Locate every Plasmodium falciparum-infected red blood cell.
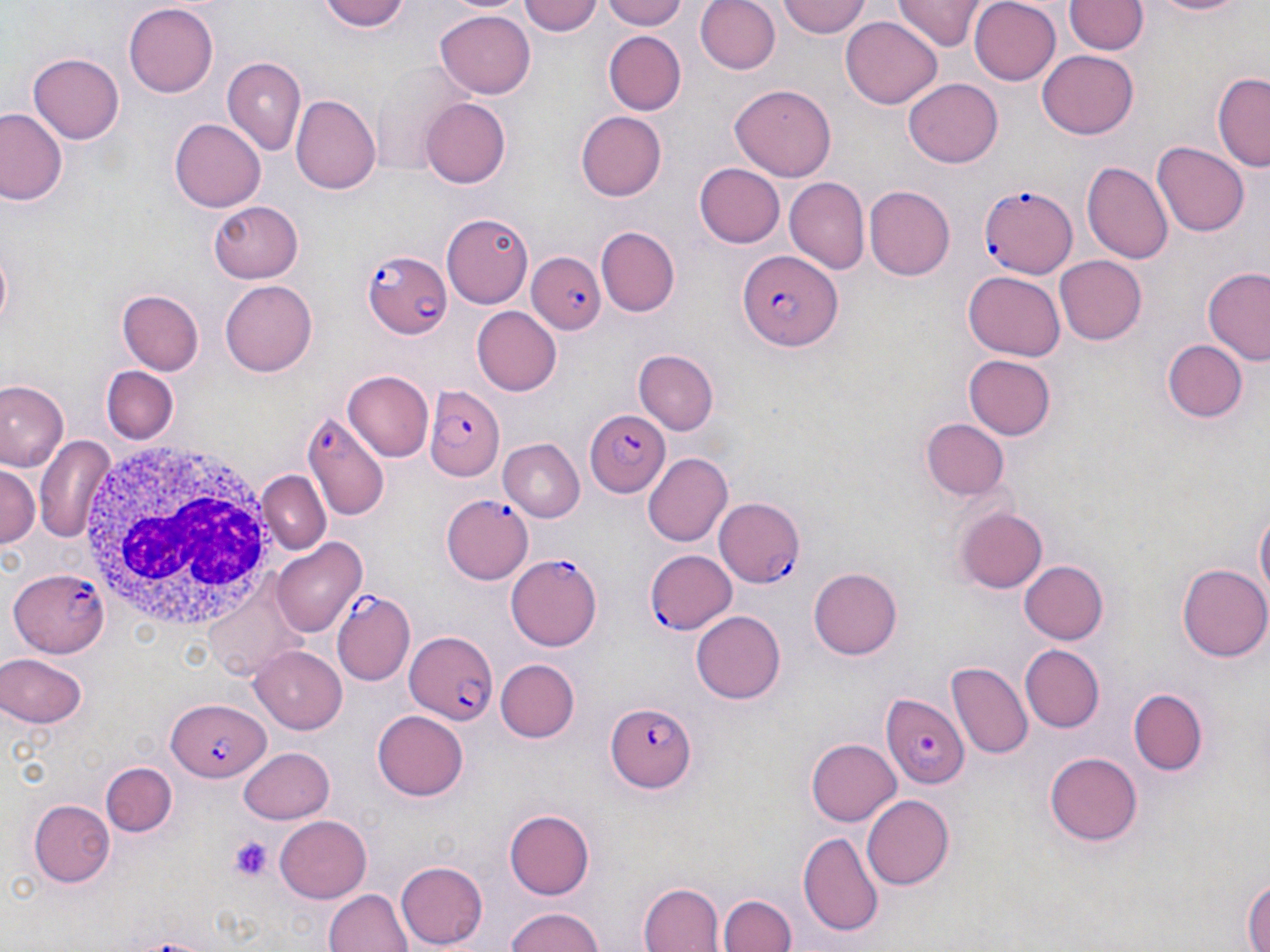

Approximate bounding boxes as named x1/y1/x2/y2 corners in pixels.
Plasmodium falciparum-infected red blood cells: (x1=979, y1=183, x2=1078, y2=278), (x1=364, y1=249, x2=453, y2=339), (x1=525, y1=250, x2=605, y2=336), (x1=735, y1=251, x2=840, y2=353), (x1=429, y1=389, x2=505, y2=481), (x1=582, y1=410, x2=670, y2=498), (x1=302, y1=416, x2=388, y2=524), (x1=441, y1=494, x2=534, y2=584), (x1=714, y1=498, x2=808, y2=588), (x1=644, y1=549, x2=737, y2=635), (x1=505, y1=555, x2=604, y2=651), (x1=7, y1=567, x2=110, y2=655), (x1=333, y1=592, x2=415, y2=686), (x1=402, y1=628, x2=498, y2=727), (x1=883, y1=694, x2=969, y2=789), (x1=167, y1=701, x2=267, y2=782), (x1=607, y1=701, x2=696, y2=793).

White blood cell locations: (x1=76, y1=436, x2=285, y2=636). Uninfected red blood cell locations: (x1=320, y1=0, x2=414, y2=33), (x1=519, y1=0, x2=604, y2=38), (x1=600, y1=0, x2=692, y2=29), (x1=695, y1=0, x2=780, y2=75), (x1=777, y1=0, x2=871, y2=38), (x1=896, y1=0, x2=983, y2=51), (x1=967, y1=0, x2=1061, y2=85), (x1=1147, y1=0, x2=1251, y2=18), (x1=1066, y1=1, x2=1146, y2=57), (x1=121, y1=3, x2=220, y2=98), (x1=436, y1=9, x2=535, y2=97), (x1=841, y1=16, x2=943, y2=109), (x1=601, y1=29, x2=687, y2=116), (x1=1037, y1=50, x2=1139, y2=140), (x1=29, y1=55, x2=123, y2=143), (x1=222, y1=57, x2=305, y2=155), (x1=367, y1=63, x2=480, y2=176), (x1=1212, y1=71, x2=1269, y2=170), (x1=903, y1=77, x2=1003, y2=168), (x1=731, y1=85, x2=837, y2=181), (x1=292, y1=94, x2=381, y2=194), (x1=421, y1=97, x2=510, y2=188), (x1=0, y1=109, x2=66, y2=207), (x1=575, y1=111, x2=668, y2=200), (x1=170, y1=118, x2=265, y2=211), (x1=1153, y1=141, x2=1249, y2=237), (x1=1084, y1=160, x2=1175, y2=265), (x1=694, y1=162, x2=783, y2=246), (x1=785, y1=177, x2=869, y2=274), (x1=865, y1=186, x2=955, y2=281), (x1=209, y1=197, x2=304, y2=281), (x1=442, y1=210, x2=533, y2=308), (x1=598, y1=225, x2=679, y2=316), (x1=1056, y1=253, x2=1146, y2=343), (x1=1200, y1=264, x2=1270, y2=364), (x1=961, y1=271, x2=1066, y2=361), (x1=221, y1=280, x2=317, y2=377), (x1=118, y1=289, x2=203, y2=375), (x1=472, y1=307, x2=562, y2=397), (x1=1162, y1=339, x2=1247, y2=423), (x1=633, y1=349, x2=719, y2=436), (x1=963, y1=352, x2=1056, y2=439), (x1=101, y1=368, x2=177, y2=445), (x1=342, y1=370, x2=434, y2=463), (x1=0, y1=380, x2=66, y2=472), (x1=921, y1=419, x2=1008, y2=500), (x1=35, y1=432, x2=116, y2=546), (x1=501, y1=439, x2=585, y2=521), (x1=644, y1=453, x2=732, y2=547), (x1=0, y1=464, x2=40, y2=551), (x1=258, y1=471, x2=330, y2=555), (x1=1253, y1=504, x2=1269, y2=610), (x1=958, y1=507, x2=1047, y2=593), (x1=272, y1=537, x2=366, y2=635), (x1=1018, y1=555, x2=1113, y2=643), (x1=1179, y1=562, x2=1270, y2=661), (x1=808, y1=567, x2=902, y2=660), (x1=692, y1=610, x2=786, y2=703), (x1=1019, y1=644, x2=1103, y2=733), (x1=252, y1=645, x2=349, y2=732), (x1=3, y1=652, x2=88, y2=728), (x1=495, y1=659, x2=580, y2=742), (x1=948, y1=661, x2=1033, y2=762), (x1=1126, y1=689, x2=1207, y2=774), (x1=374, y1=710, x2=468, y2=800), (x1=806, y1=738, x2=901, y2=826), (x1=239, y1=744, x2=335, y2=823), (x1=1046, y1=750, x2=1144, y2=845), (x1=100, y1=763, x2=177, y2=839), (x1=862, y1=795, x2=955, y2=889), (x1=29, y1=799, x2=113, y2=886), (x1=504, y1=809, x2=595, y2=899), (x1=276, y1=814, x2=372, y2=901), (x1=799, y1=832, x2=884, y2=936), (x1=394, y1=859, x2=489, y2=948), (x1=1244, y1=873, x2=1269, y2=952), (x1=638, y1=881, x2=725, y2=952), (x1=323, y1=887, x2=412, y2=952), (x1=719, y1=890, x2=795, y2=952), (x1=504, y1=906, x2=608, y2=952). Platelet locations: (x1=227, y1=838, x2=275, y2=881). Slide-level diagnosis: Plasmodium falciparum. May-Grünwald-Giemsa-stained preparation. Light microscopy. Captured at 1000x magnification. Image is 1270×952 pixels. Thin blood film. One field of a larger specimen.